Identify the cell.
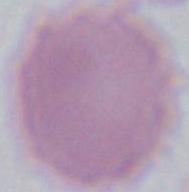

This is an erythrocyte.

Summary:
  - Magnification: 1000x
  - Modality: micrograph